Identify the cell.
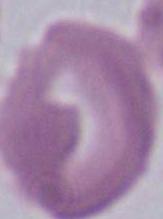

An erythrocyte.

1000x magnification. Micrograph.